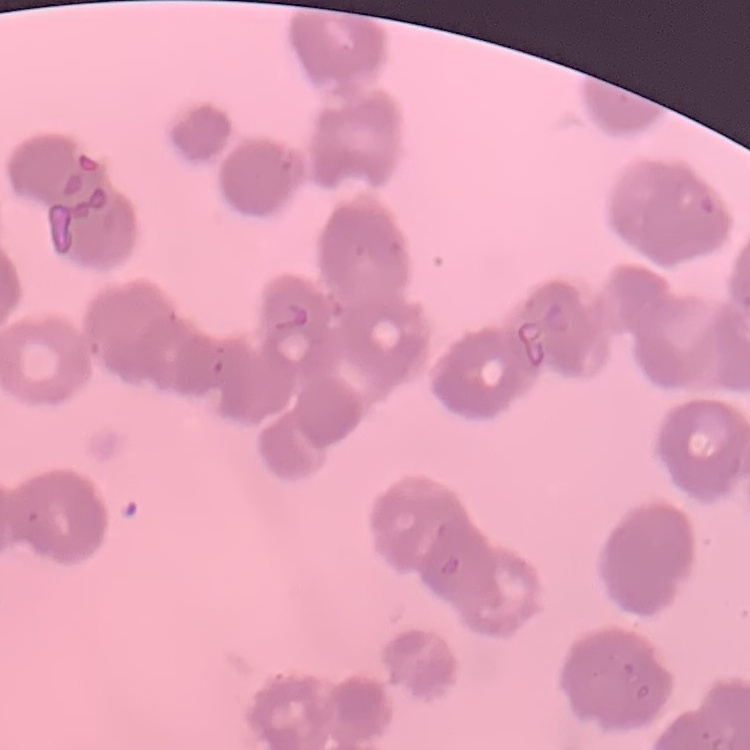

red_blood_cell_morphology: rouleaux formation
preparation: thin blood smear
image_type: square crop of a larger photomicrograph
stain: Field's or Giemsa